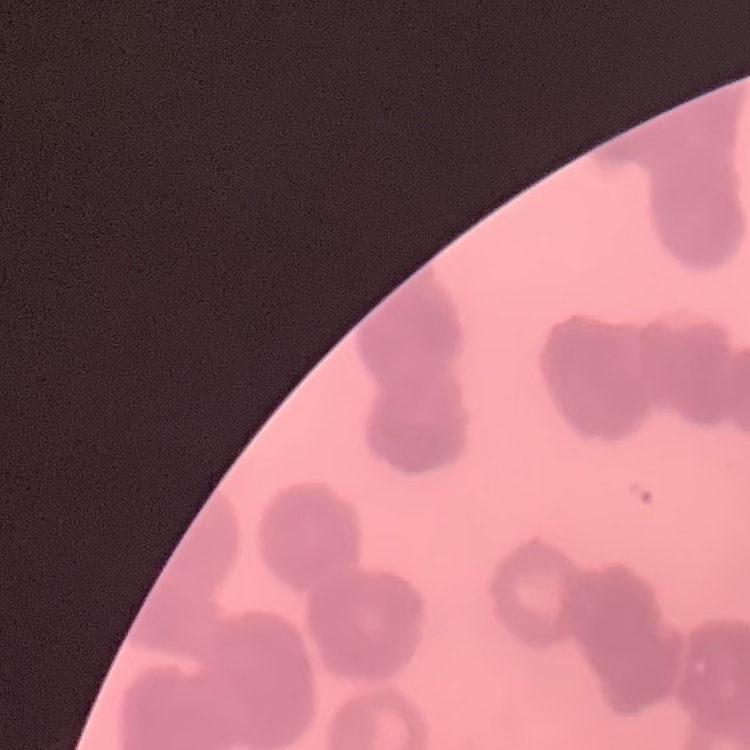

The erythrocytes show rouleaux formation. Field's or Giemsa stain. Thin blood film. One tile cut from a larger photomicrograph.